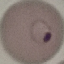
Result: malaria parasites detected. Cell patch, automatically extracted from a larger field of view and resized to 64 × 64 pixels. Giemsa stain. Photographed with a smartphone camera at the microscope eyepiece. Thin blood film.